Give the extent of all Plasmodium malariae-infected red blood cells.
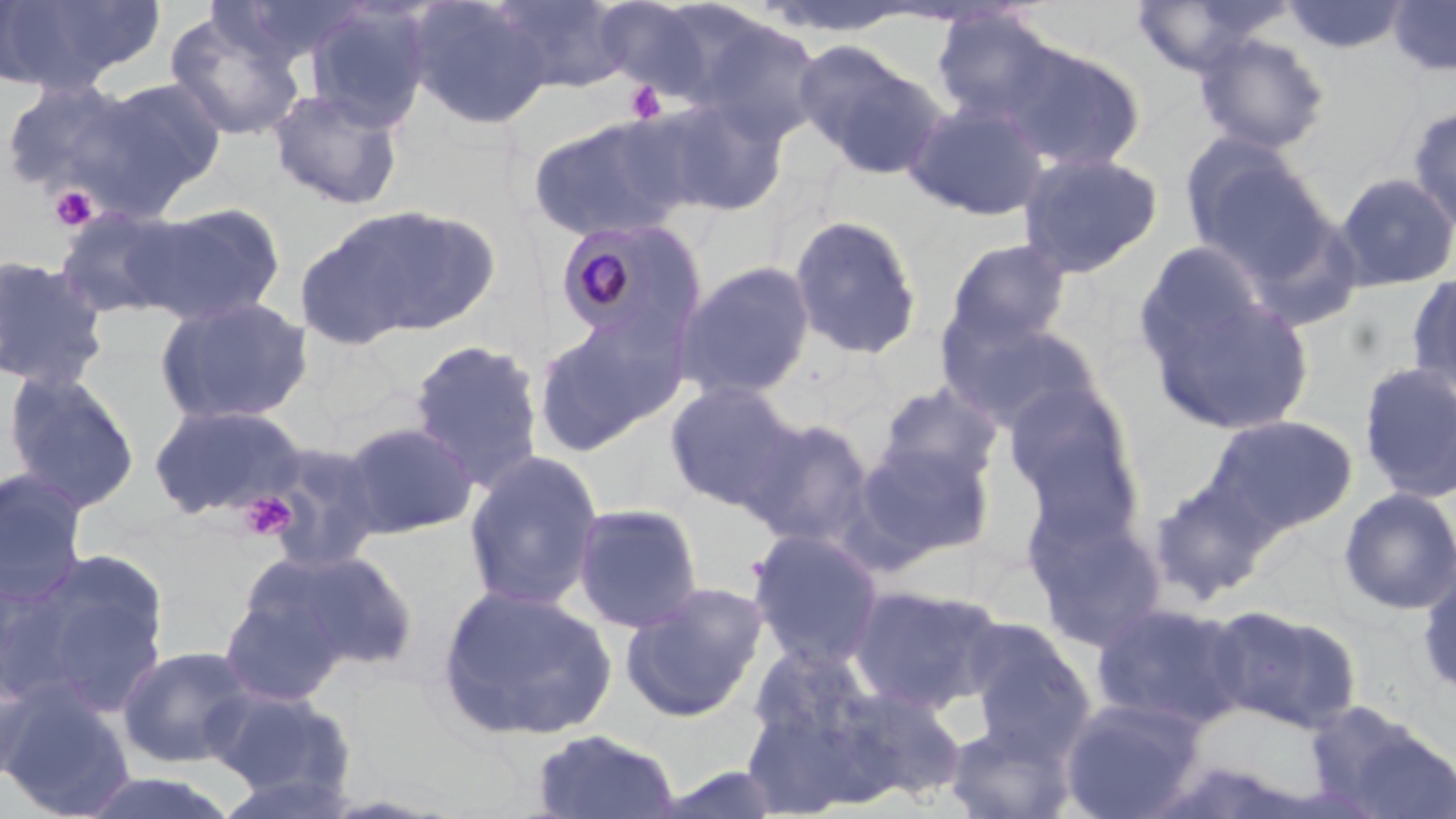

Approximate bounding boxes as (x1,y1)-(x2,y2) corner pairs in pixels.
Plasmodium malariae-infected red blood cells: (553,218)-(697,345).

Summary:
  - Platelet locations: (626,81)-(666,125), (48,185)-(99,233), (237,491)-(299,542)
  - Uninfected red blood cell locations: (0,0)-(161,94), (405,0)-(554,131), (491,0)-(633,93), (596,0)-(732,100), (748,0)-(923,39), (1130,0)-(1284,78), (1283,0)-(1408,54), (1387,0)-(1456,76), (302,2)-(434,131), (931,8)-(1063,127), (164,9)-(306,143), (690,12)-(827,145), (1193,31)-(1332,156), (998,40)-(1146,172), (800,46)-(947,180), (64,77)-(226,220), (0,78)-(137,195), (267,87)-(406,211), (651,95)-(789,217), (904,97)-(1049,221), (1407,105)-(1456,234), (526,113)-(694,243), (1182,138)-(1328,275), (1017,150)-(1164,279), (1333,171)-(1456,293), (127,202)-(287,326), (321,203)-(502,340), (54,206)-(188,320), (788,213)-(923,360), (944,238)-(1072,352), (1135,239)-(1271,368), (0,254)-(111,391), (673,259)-(816,402), (1406,270)-(1456,399), (1148,293)-(1316,436), (153,296)-(314,426), (942,315)-(1106,436), (531,320)-(668,457), (407,338)-(545,492), (1357,362)-(1456,504), (2,369)-(142,514), (665,380)-(800,511), (1004,381)-(1145,531), (874,382)-(1004,492), (147,401)-(308,520), (1203,414)-(1357,536), (739,416)-(876,549), (338,420)-(479,539), (854,439)-(995,562), (256,440)-(387,572), (462,450)-(605,612), (0,468)-(90,602), (1147,472)-(1273,605), (1338,487)-(1456,615), (571,502)-(704,633), (1025,504)-(1170,652), (747,528)-(886,670), (275,548)-(421,674), (14,556)-(172,711), (1416,564)-(1456,701), (620,580)-(770,722), (435,583)-(618,742), (847,583)-(1005,715), (217,588)-(349,707), (1091,600)-(1250,731), (1205,604)-(1362,734), (963,618)-(1095,755), (116,644)-(256,769), (0,661)-(42,785), (742,665)-(912,815), (828,683)-(967,803), (204,685)-(357,802), (0,688)-(136,818), (1060,697)-(1208,818), (1305,700)-(1454,818), (942,723)-(1076,818), (529,728)-(682,819), (71,770)-(241,818)
  - Slide-level diagnosis: Plasmodium malariae
  - Image size: 1456×819 pixels
  - Stain: May-Grünwald-Giemsa
  - Preparation: thin blood smear
  - Modality: optical microscopy
  - Magnification: 1000x
  - Field of view: single